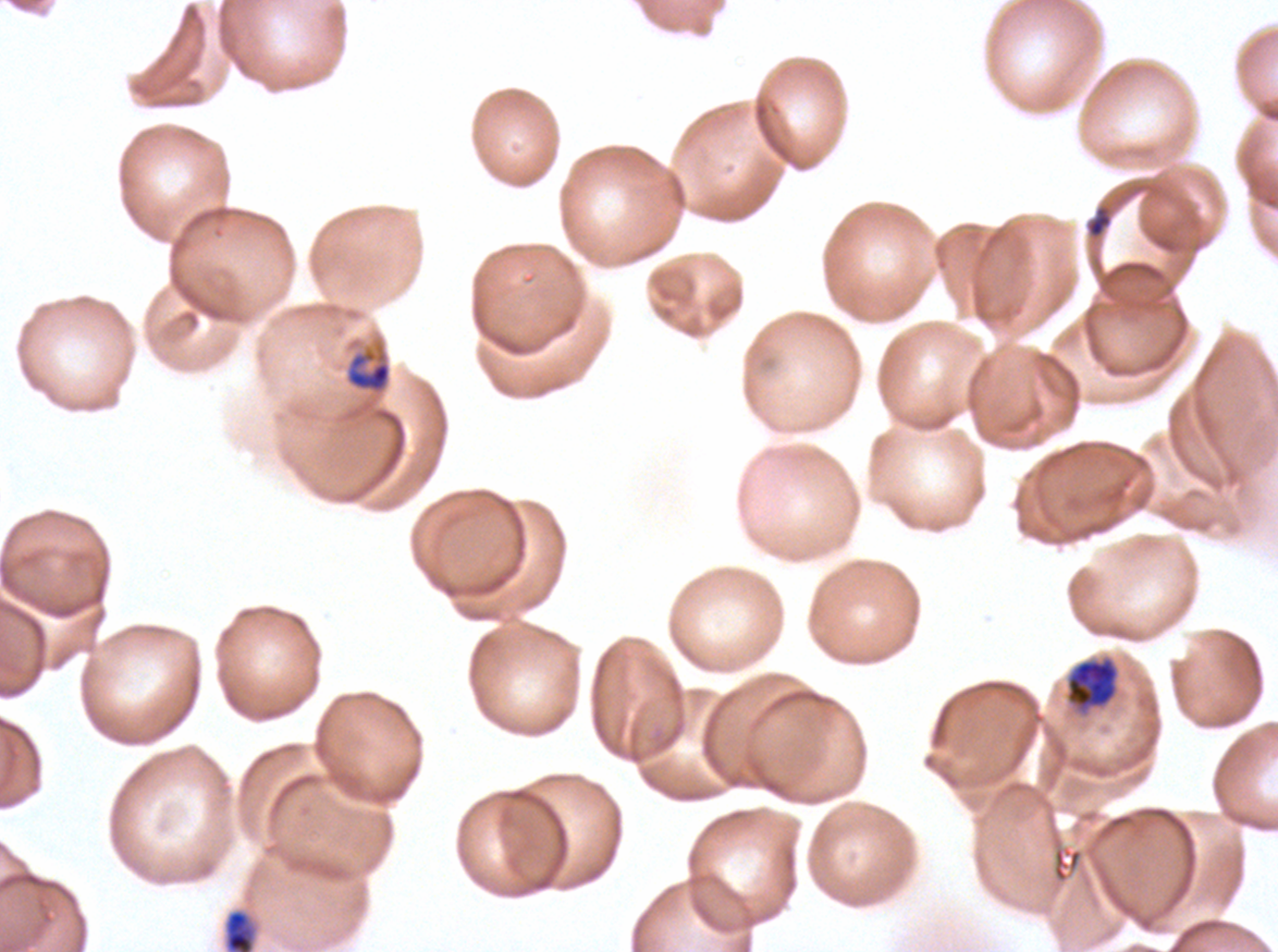

Approximate bounding boxes as [x1, y1, x2, y2] in pixels. Mid trophozoite locations: [345, 344, 392, 395]. Late-ring/early-trophozoite locations: [223, 909, 257, 951]. Late trophozoite locations: [1065, 657, 1119, 711]. Debris locations: [1086, 205, 1112, 239]. Image is 1278×952 pixels. Life-cycle stages observed: late-ring/early-trophozoite, mid trophozoite, late trophozoite. Thin blood film. P. falciparum from a patient in The Gambia, cultured ex vivo for 24 to 48 hours. A sub-image separated from a larger composite. Giemsa stain.